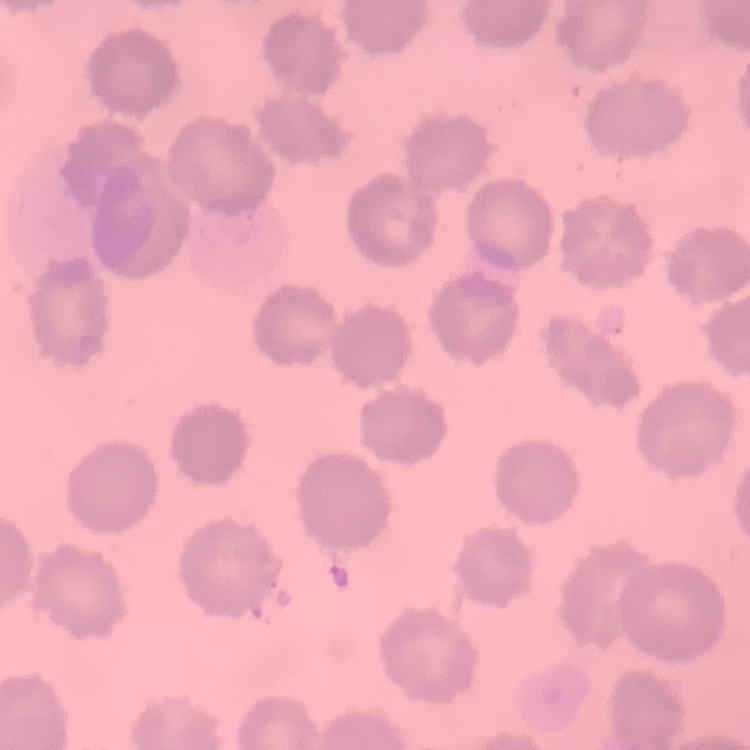
Summary:
  - Erythrocyte morphology: no rouleaux formation
  - Image type: one tile cut from a larger photomicrograph
  - Preparation: thin peripheral smear
  - Stain: Field's or Giemsa